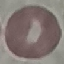
Result: no malaria parasites detected. Giemsa stain. Photographed with a smartphone camera at the microscope eyepiece. Automatically extracted cell patch, resized to 64 × 64 pixels. Thin smear of blood.